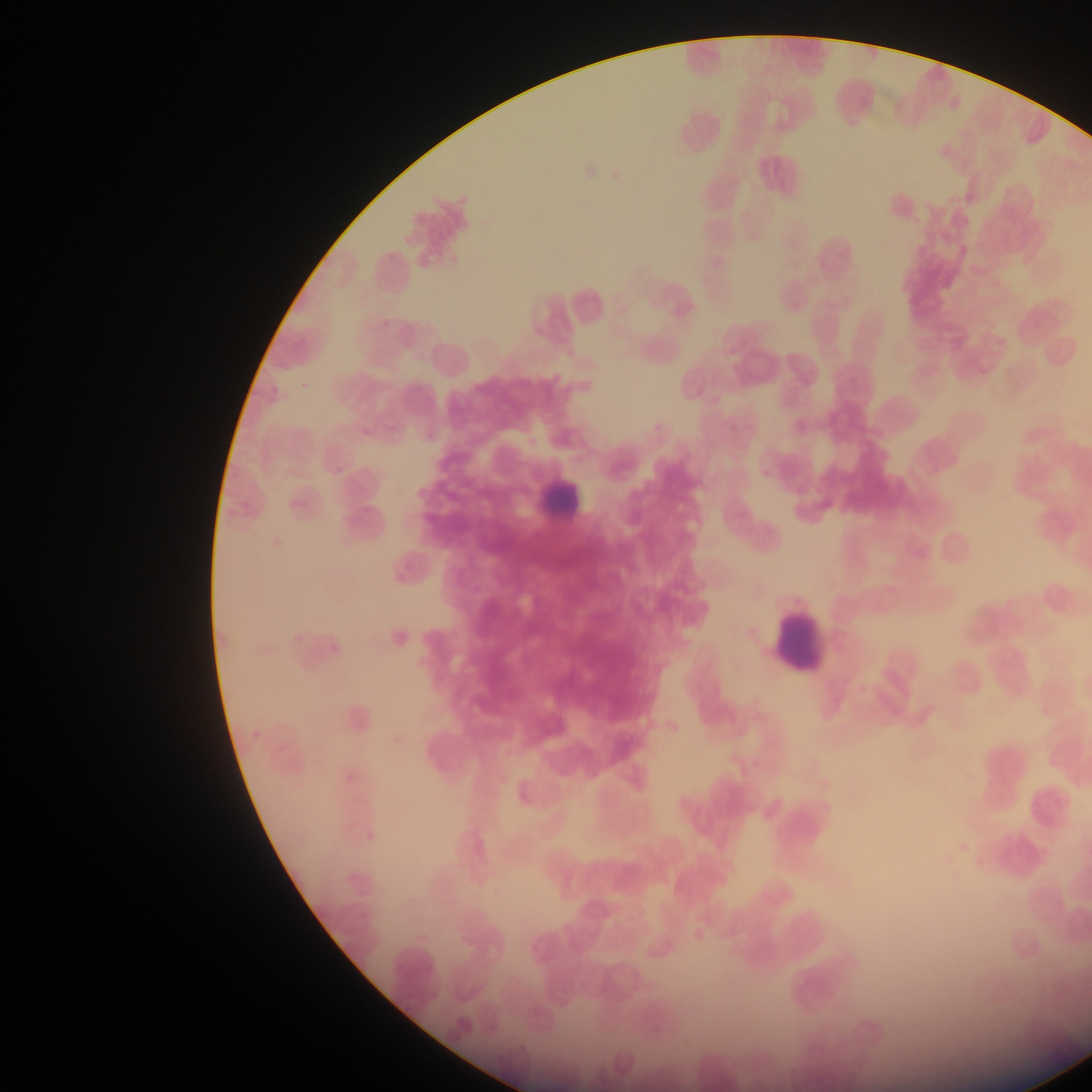
Approximate bounding boxes as [left, top, right, bottom] in pixels.
Summary:
  - Leukocyte locations: [536, 466, 590, 526], [773, 610, 830, 673]
  - Field of view: single
  - Country: Ghana
  - Preparation: thin blood film
  - Capture: mobile-phone photograph through a microscope
  - Image size: 1092×1092 pixels